Assess this cell for malaria.
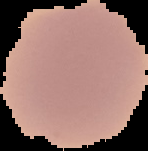

Uninfected.

preparation = thin blood smear
image size = 148×151 pixels
image type = cell region segmented out of the field of view; surrounding area masked to black